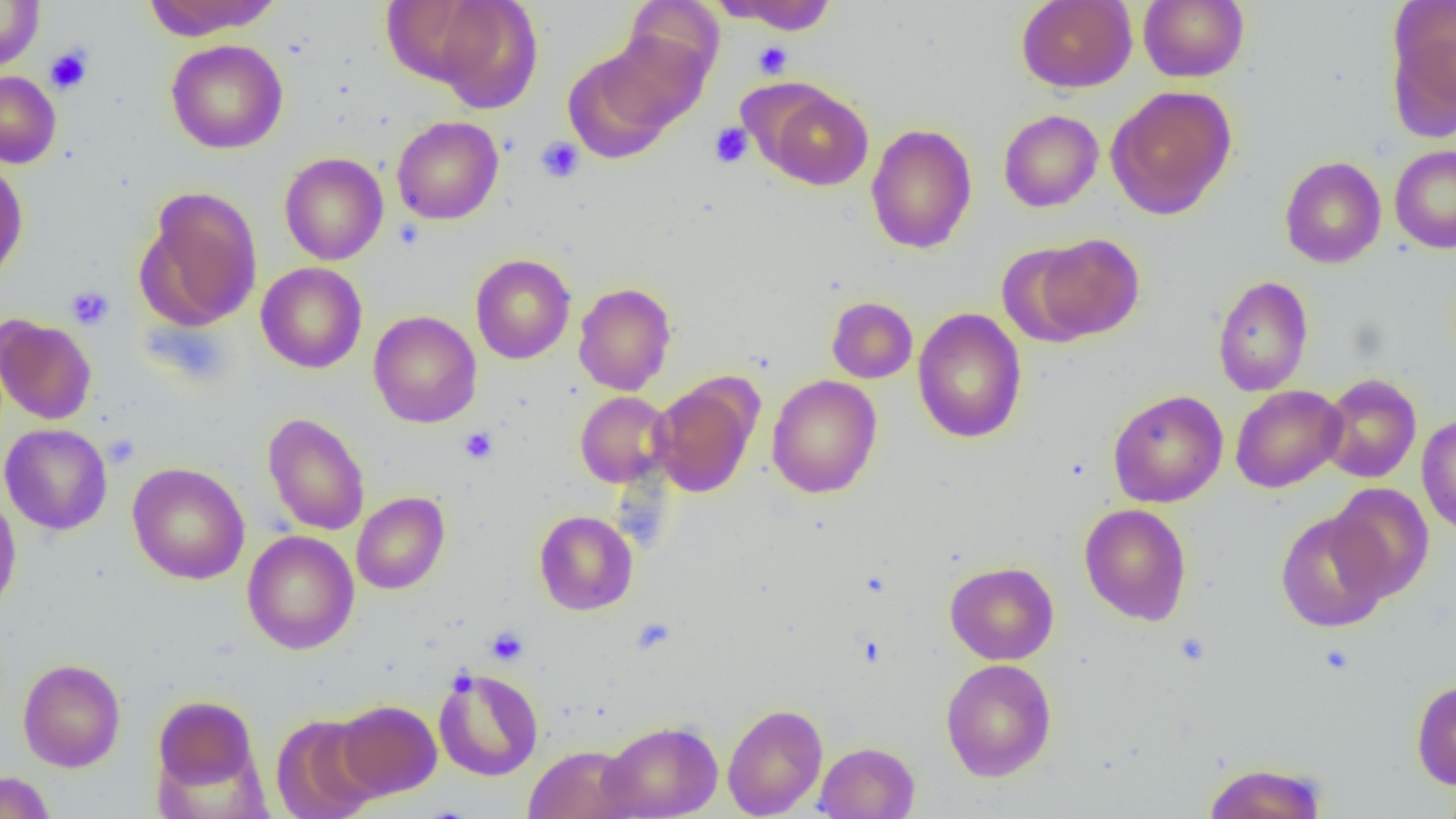

Approximate bounding boxes as [x1, y1, x2, y2] in pixels. Uninfected red blood cell locations: [0, 0, 45, 73], [142, 0, 281, 40], [427, 0, 544, 113], [716, 0, 839, 35], [1386, 0, 1456, 132], [622, 1, 723, 88], [1016, 1, 1137, 93], [1138, 1, 1249, 83], [596, 32, 709, 133], [166, 39, 288, 154], [562, 47, 682, 163], [0, 71, 61, 168], [1106, 85, 1237, 220], [763, 86, 873, 191], [998, 109, 1103, 212], [391, 116, 504, 224], [865, 123, 977, 254], [1389, 144, 1456, 254], [279, 152, 388, 266], [1279, 156, 1386, 269], [0, 160, 28, 286], [137, 187, 263, 332], [1027, 234, 1145, 343], [996, 242, 1100, 348], [470, 254, 575, 364], [256, 262, 368, 373], [1212, 275, 1313, 397], [573, 282, 676, 395], [826, 297, 918, 383], [912, 308, 1027, 444], [369, 310, 482, 428], [0, 314, 97, 425], [1319, 373, 1421, 483], [767, 375, 882, 499], [650, 378, 760, 497], [1230, 384, 1347, 493], [1107, 390, 1228, 507], [575, 391, 675, 487], [262, 412, 370, 536], [1417, 413, 1456, 536], [0, 423, 113, 535], [127, 462, 250, 585], [1327, 483, 1435, 603], [0, 489, 22, 619], [352, 491, 450, 594], [1079, 503, 1192, 625], [1276, 510, 1392, 632], [534, 511, 638, 615], [242, 530, 359, 654], [945, 561, 1059, 665], [18, 658, 126, 772], [940, 658, 1057, 782], [432, 666, 544, 782], [1411, 679, 1456, 789], [153, 695, 259, 791], [336, 700, 442, 800], [722, 703, 828, 818], [270, 713, 382, 818], [598, 720, 723, 818], [815, 741, 919, 819], [524, 745, 637, 819], [1201, 761, 1329, 819], [0, 771, 55, 819], [1440, 776, 1456, 819]. Platelet locations: [753, 41, 792, 78], [44, 44, 93, 95], [709, 123, 753, 168], [536, 137, 584, 182], [66, 287, 114, 330], [459, 427, 498, 464], [103, 435, 140, 468], [632, 616, 676, 654], [485, 626, 529, 666], [1174, 631, 1211, 666], [1319, 643, 1355, 675]. Slide-level diagnosis: negative for blood parasites. Thin blood smear. Light microscopy. Image is 1456×819 pixels. One field of a larger specimen. Captured at 1000x magnification.